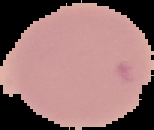

result = no malaria parasites seen
preparation = thin blood film
image size = 154×130 pixels
image type = segmented cell region on a black background